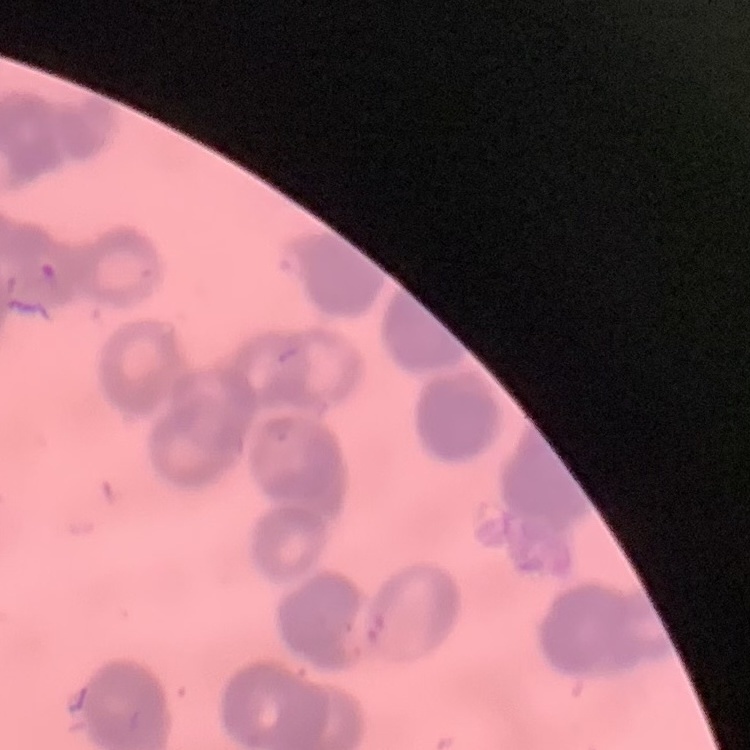

The erythrocytes show rouleaux formation. Stained with either Field's or Giemsa. Thin blood film. One tile cut from a larger photomicrograph.